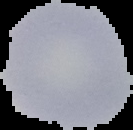
image size = 133×130 pixels
malaria status = uninfected
image type = segmented cell region on a black background
preparation = thin blood film